Assess the morphology of the red blood cells.
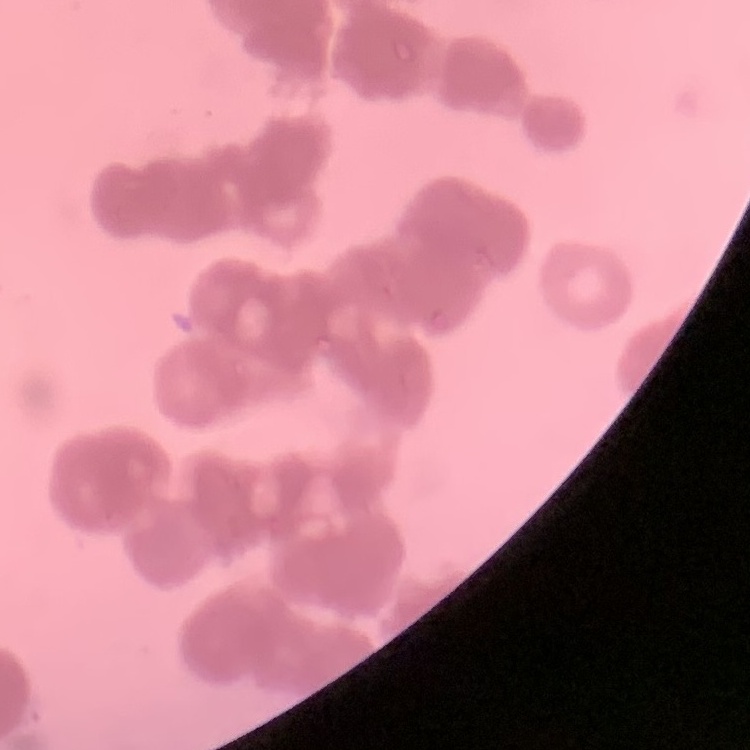

They show rouleaux formation.

Summary:
  - Image type: one tile cut from a larger photomicrograph
  - Preparation: thin blood smear
  - Stain: Field's or Giemsa